Give the extent of all uninfected red blood cells.
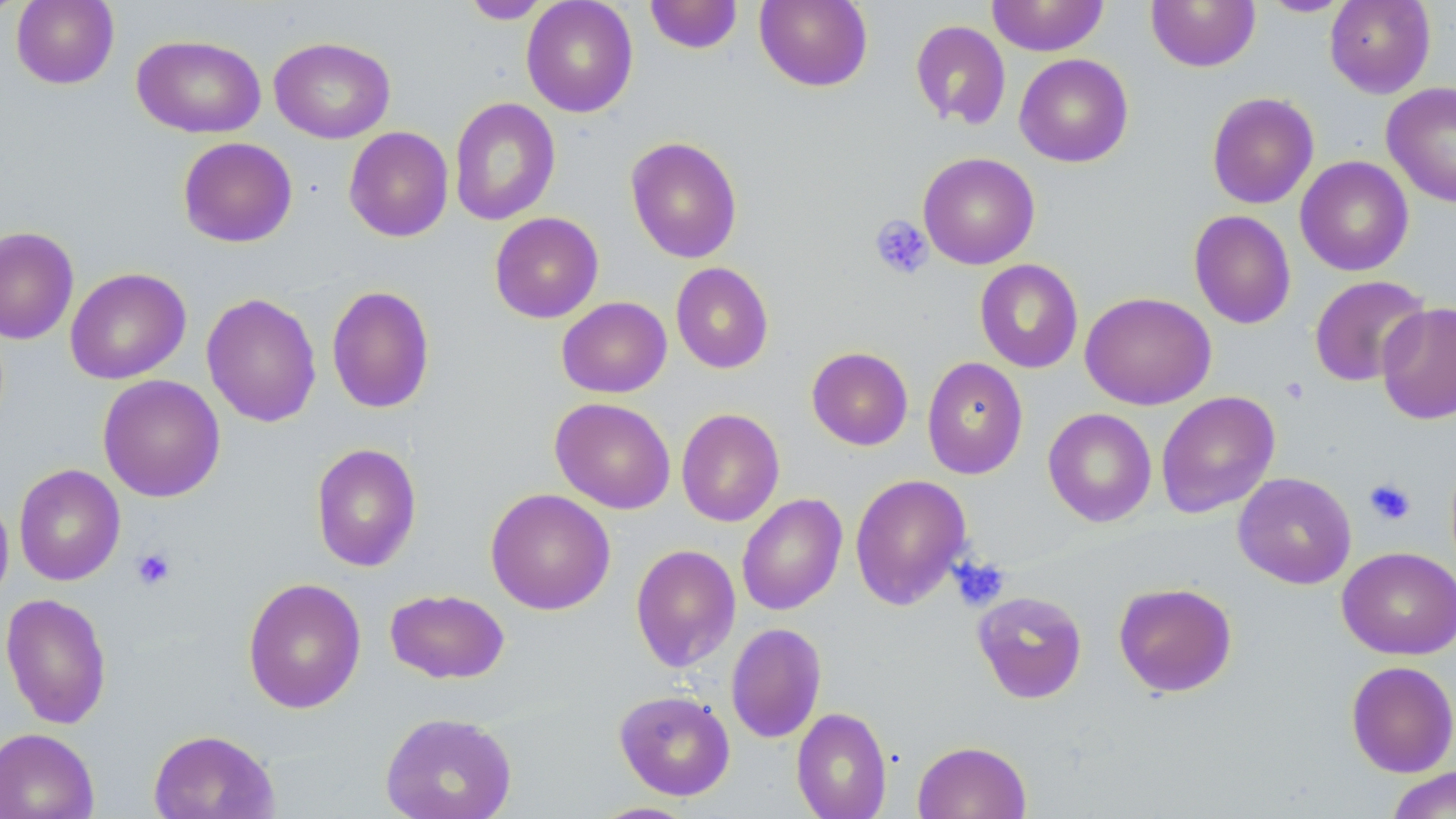

Approximate bounding boxes as [x1, y1, x2, y2] in pixels.
Uninfected red blood cells: [0, 0, 24, 22], [11, 0, 119, 89], [460, 0, 553, 24], [521, 0, 638, 117], [646, 0, 743, 54], [754, 0, 873, 92], [987, 0, 1109, 56], [1146, 0, 1261, 72], [1324, 0, 1436, 98], [1258, 1, 1353, 17], [910, 20, 1011, 130], [132, 34, 266, 138], [269, 36, 396, 143], [1014, 53, 1133, 167], [1382, 82, 1456, 208], [1207, 92, 1319, 209], [449, 97, 560, 226], [343, 126, 453, 242], [625, 136, 743, 264], [177, 137, 298, 248], [917, 152, 1040, 270], [1295, 156, 1413, 276], [1188, 210, 1296, 329], [489, 212, 604, 323], [0, 226, 79, 345], [974, 259, 1084, 373], [671, 262, 774, 374], [65, 267, 191, 385], [1309, 275, 1430, 387], [326, 285, 435, 414], [1080, 291, 1216, 410], [201, 292, 322, 428], [557, 297, 671, 398], [1376, 301, 1456, 426], [806, 346, 913, 451], [922, 357, 1029, 480], [97, 374, 226, 502], [1156, 391, 1280, 518], [550, 397, 676, 514], [676, 408, 785, 527], [1043, 408, 1157, 527], [311, 443, 421, 572], [13, 464, 125, 586], [1232, 471, 1357, 589], [850, 474, 973, 610], [485, 488, 615, 615], [0, 491, 13, 610], [736, 493, 848, 616], [630, 543, 741, 673], [1337, 547, 1456, 659], [242, 577, 366, 714], [1113, 582, 1238, 697], [385, 589, 510, 684], [972, 590, 1088, 703], [1, 592, 113, 729], [725, 623, 827, 743], [1345, 660, 1456, 777], [614, 689, 736, 801], [791, 706, 892, 819], [380, 712, 518, 819], [0, 728, 99, 819], [148, 729, 280, 819], [913, 740, 1031, 819], [1385, 767, 1455, 818], [588, 801, 699, 819].

Platelet locations: [869, 214, 933, 280], [1364, 478, 1416, 526], [132, 546, 176, 590], [950, 557, 1011, 610]. Slide-level diagnosis: no evidence of blood parasites. Captured at 1000x magnification. Light microscopy. Thin blood smear. One field of a larger specimen. May-Grünwald-Giemsa stain. Image is 1456×819 pixels.